Locate every blood parasite and identify its species.
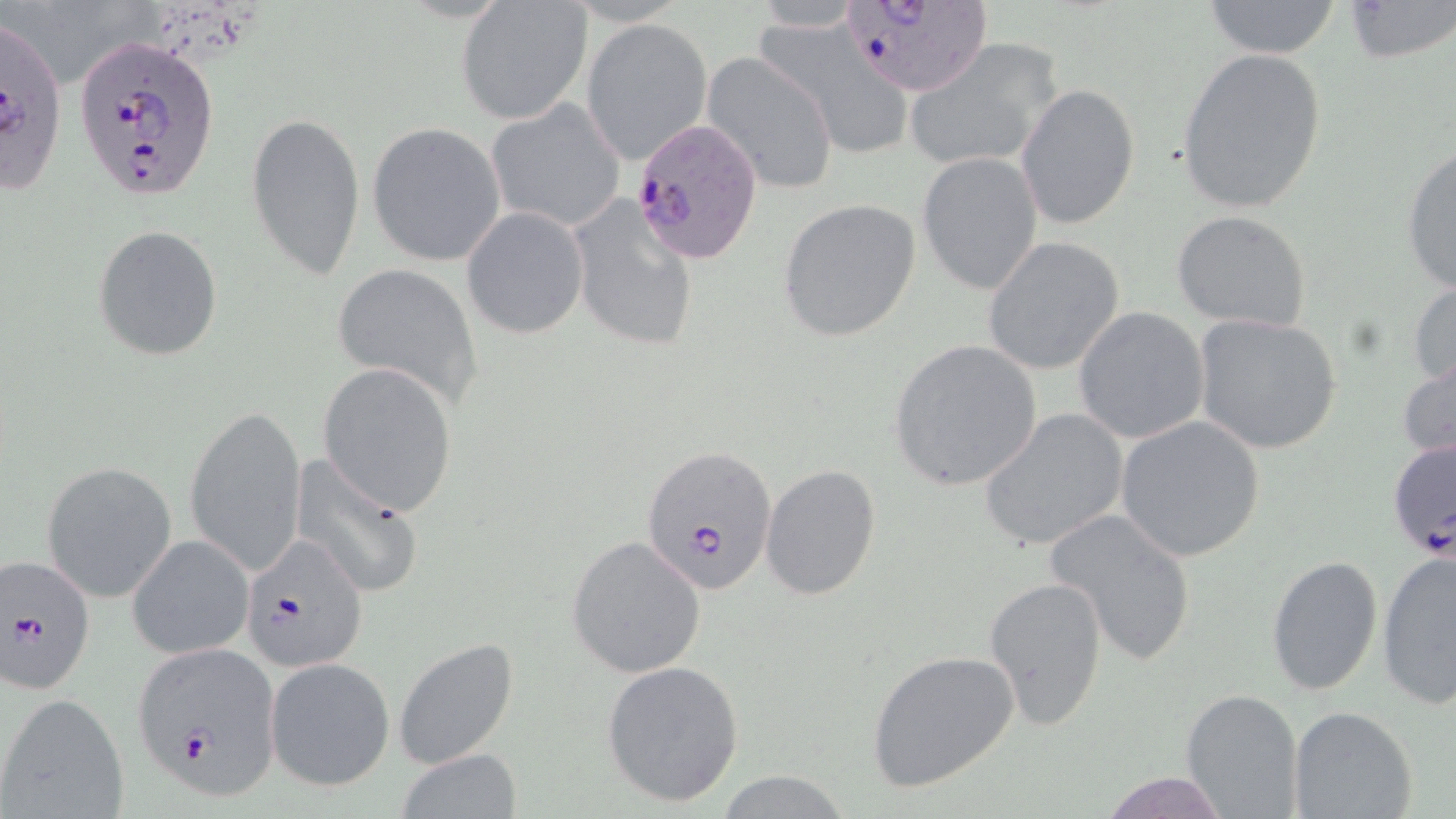
Approximate bounding boxes as (x1,y1)-(x2,y2) corner pairs in pixels.
Plasmodium falciparum-infected red blood cells: (834,0)-(992,98), (0,17)-(67,196), (74,34)-(222,203), (629,115)-(765,266), (1395,436)-(1456,567), (641,444)-(779,597), (242,534)-(367,671), (2,553)-(96,694), (133,644)-(283,804).
No Plasmodium ovale, Plasmodium malariae, Plasmodium vivax, Babesia divergens, or Trypanosoma brucei observed.

Summary:
  - Uninfected red blood cell locations: (1342,0)-(1454,63), (1199,1)-(1344,59), (455,3)-(593,124), (581,19)-(712,163), (754,19)-(912,155), (905,36)-(1063,173), (1175,48)-(1328,214), (701,52)-(839,196), (1017,83)-(1140,231), (485,98)-(626,233), (245,109)-(366,281), (367,123)-(507,267), (1399,144)-(1456,297), (917,150)-(1043,295), (567,195)-(700,353), (777,198)-(922,342), (461,207)-(589,340), (1171,210)-(1314,332), (91,224)-(224,360), (983,239)-(1124,375), (332,264)-(485,412), (1408,277)-(1456,392), (1073,306)-(1209,444), (1192,314)-(1342,454), (886,338)-(1043,494), (1397,351)-(1456,466), (318,362)-(459,516), (187,404)-(307,580), (979,409)-(1128,551), (1115,416)-(1266,562), (290,457)-(425,598), (42,461)-(177,602), (761,464)-(883,601), (1045,507)-(1196,668), (127,534)-(254,660), (567,535)-(705,678), (1377,549)-(1456,709), (1265,554)-(1383,697), (984,574)-(1108,731), (393,636)-(521,770), (866,649)-(1021,793), (266,657)-(395,791), (600,660)-(745,807), (1180,688)-(1304,818), (1,693)-(131,819), (1288,704)-(1418,819), (395,749)-(521,819), (1100,769)-(1231,819), (716,771)-(854,817)
  - Slide-level diagnosis: Plasmodium falciparum
  - Field of view: one of a larger specimen
  - Image size: 1456×819 pixels
  - Stain: May-Grünwald-Giemsa
  - Magnification: 1000x
  - Modality: light microscopy
  - Preparation: thin blood smear